Name the parasite shown.
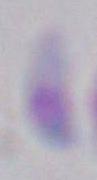

Toxoplasma gondii.

Summary:
  - Modality: photomicrograph
  - Magnification: 1000x